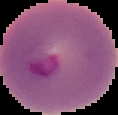 The area outside the segmented cell region is set to black. Malaria status: parasitized. From a thin blood smear. Image is 118×115 pixels.